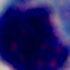

Summary:
  - Identification: white blood cell
  - Magnification: 1000x
  - Modality: micrograph